Assess this cell for malaria.
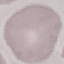

Uninfected.

preparation = thin smear
capture = smartphone through the microscope eyepiece
stain = Giemsa
image type = automatically extracted cell patch, resized to 64 × 64 pixels